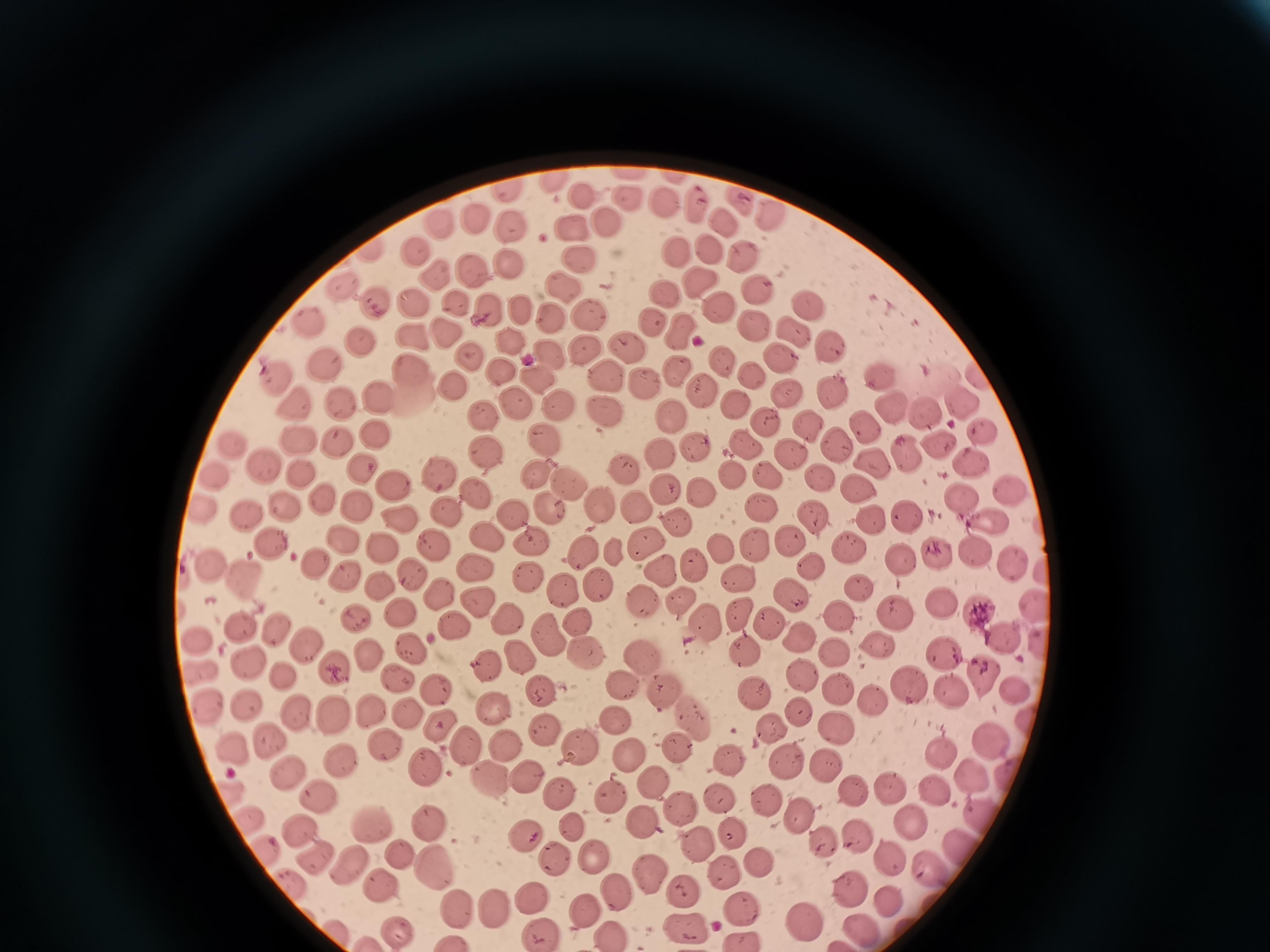

Approximate centers as (x, y) in pixels. Cell locations: (553, 186), (508, 193), (585, 198), (664, 202), (693, 203), (480, 218), (722, 220), (442, 224), (607, 224), (512, 228), (572, 229), (418, 246), (712, 249), (678, 250), (745, 254), (578, 260), (509, 267), (472, 270), (437, 277), (699, 280), (346, 283), (564, 285), (759, 287), (668, 290), (416, 298), (380, 302), (455, 304), (809, 304), (492, 305), (714, 306), (526, 313), (590, 313), (555, 316), (654, 316), (750, 322), (313, 323), (451, 329), (682, 330), (793, 330), (413, 332), (511, 341), (363, 342), (831, 344), (629, 347), (584, 348), (549, 349), (781, 355), (474, 356), (324, 362), (724, 362), (415, 364), (501, 368), (676, 368), (274, 370), (880, 373), (979, 373), (534, 374), (604, 374), (751, 375), (449, 383), (642, 387), (833, 389), (701, 392), (785, 393), (379, 395), (336, 396), (289, 397), (964, 399), (558, 402), (516, 404), (734, 404), (893, 404), (602, 412), (670, 413), (927, 413), (487, 415), (764, 422), (807, 424), (863, 425), (985, 427), (375, 436), (543, 436), (300, 441), (836, 442), (340, 443), (745, 443), (234, 444), (694, 444), (939, 444), (486, 447), (658, 451), (906, 451), (792, 454), (870, 460), (973, 462), (269, 466), (364, 466), (623, 467), (443, 472), (538, 472), (216, 475), (733, 475), (817, 475), (304, 477), (767, 478), (392, 483), (570, 486), (1010, 488), (665, 489), (855, 489), (477, 491), (696, 493), (327, 497), (961, 498), (358, 502), (601, 504), (202, 505), (285, 505), (762, 506), (638, 508), (446, 509), (551, 510), (517, 513), (399, 514), (866, 515), (904, 515), (814, 516), (244, 518), (676, 519), (991, 519), (488, 535), (345, 537), (792, 537), (643, 539), (270, 540), (755, 540), (533, 542), (434, 543), (850, 544), (384, 547), (974, 547), (721, 549), (582, 550), (939, 551), (618, 553), (1014, 558), (211, 559), (903, 559), (691, 561), (810, 561), (318, 562), (477, 566), (665, 570), (413, 572), (348, 573), (250, 575), (739, 575), (529, 578), (598, 583), (858, 585), (382, 586), (566, 588), (440, 593), (790, 594), (478, 600), (643, 600), (682, 601), (943, 602), (981, 610), (356, 612), (401, 612), (741, 615), (896, 616), (838, 617), (510, 619), (575, 619), (454, 624), (705, 624), (774, 624), (242, 628), (279, 631), (548, 635), (800, 636), (1003, 636), (197, 638), (879, 643), (408, 644), (308, 647), (838, 649), (944, 650), (744, 652), (370, 653), (585, 653), (518, 655), (642, 658), (248, 661), (489, 663), (198, 671), (336, 672), (978, 674), (286, 676), (801, 677), (400, 678), (620, 680), (836, 686), (436, 687), (910, 687), (663, 688), (548, 690), (757, 692), (952, 693), (1013, 694), (875, 701), (249, 702), (204, 705), (369, 710), (493, 710), (798, 710), (299, 712), (405, 712), (333, 714), (618, 717), (694, 717), (439, 726), (839, 726), (768, 728), (546, 732), (268, 737), (465, 740), (992, 742), (507, 743), (576, 744), (384, 746), (681, 749), (236, 753), (941, 753), (630, 757), (337, 760), (731, 761), (783, 762), (425, 765), (825, 765), (287, 769), (485, 774), (970, 774), (524, 775), (1005, 776), (654, 783), (889, 788), (852, 789), (936, 791), (229, 792), (319, 792), (557, 793), (721, 793), (608, 796), (768, 800), (677, 813), (978, 813), (799, 815), (371, 818), (250, 820), (644, 821), (910, 822), (300, 823), (429, 829), (578, 831), (524, 834), (734, 837), (822, 838), (857, 840), (698, 846), (958, 847), (262, 848), (402, 851), (313, 852), (595, 855), (558, 860), (891, 861), (765, 862), (352, 867), (434, 868), (932, 868), (648, 869), (724, 872), (292, 880), (379, 884), (851, 885), (684, 888), (614, 891), (533, 896), (891, 904), (494, 906), (583, 909), (743, 911), (460, 913), (804, 916), (687, 925), (394, 929), (865, 929), (541, 932), (611, 935). Photographed with a smartphone camera at the microscope eyepiece. Single field of view. Image is 1270×952 pixels. Thin blood film. Giemsa stain.